Classify this cell by malaria status.
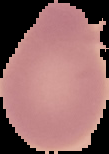

It is uninfected.

From a thin blood smear. Image is 109×154 pixels. The area outside the segmented cell region is set to black.